Describe the morphology of the red blood cells.
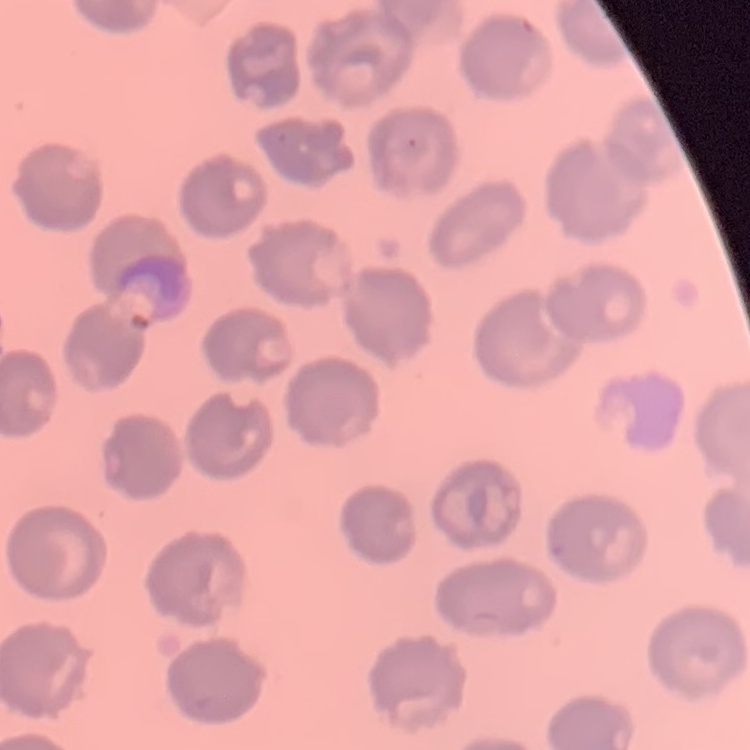

They show no rouleaux formation.

{
  "image_type": "square crop of a larger photomicrograph",
  "stain": "Field's or Giemsa",
  "preparation": "thin peripheral smear"
}